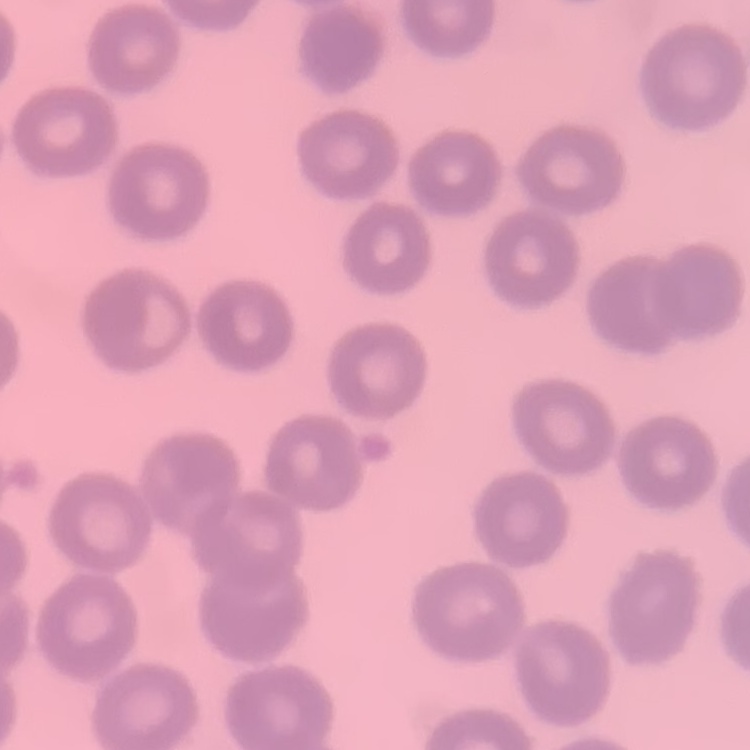
erythrocyte morphology = no rouleaux formation
stain = Field's or Giemsa
image type = one tile cut from a larger photomicrograph
preparation = thin blood smear